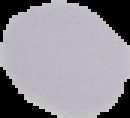

Summary:
  - Image type: segmented cell region with the area outside set to black
  - Malaria status: uninfected
  - Image size: 130×118 pixels
  - Preparation: thin blood smear